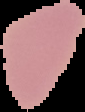
Summary:
  - Result: negative for malaria parasites
  - Image type: cell region segmented out of the field of view; surrounding area masked to black
  - Preparation: thin blood film
  - Image size: 85×112 pixels